Describe the morphology of the red blood cells.
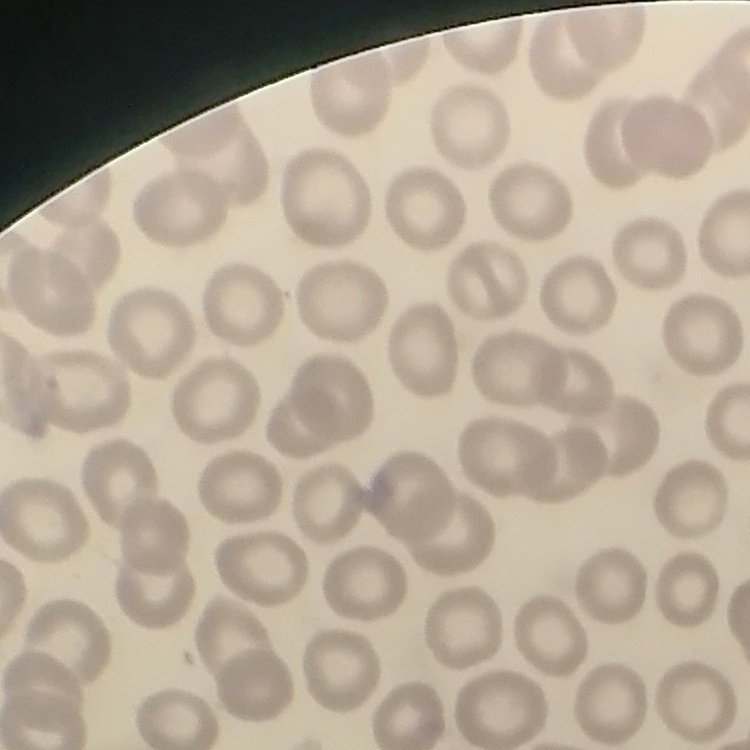
No rouleaux formation.

preparation = thin peripheral smear
image type = square crop of a larger photomicrograph
stain = Field's or Giemsa